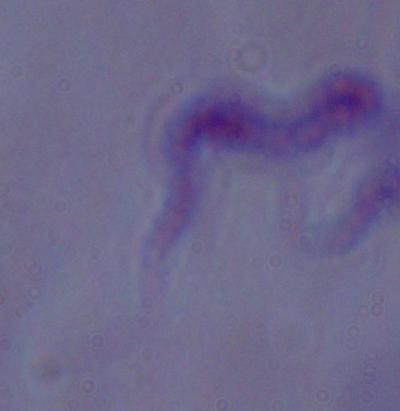
Summary:
  - Modality: micrograph
  - Magnification: 1000x
  - Identification: trypanosome